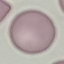

result = no malaria parasites seen
image type = cell patch, automatically extracted from a larger field of view and resized to 64 × 64 pixels
capture = smartphone through the microscope eyepiece
preparation = thin blood film
stain = Giemsa